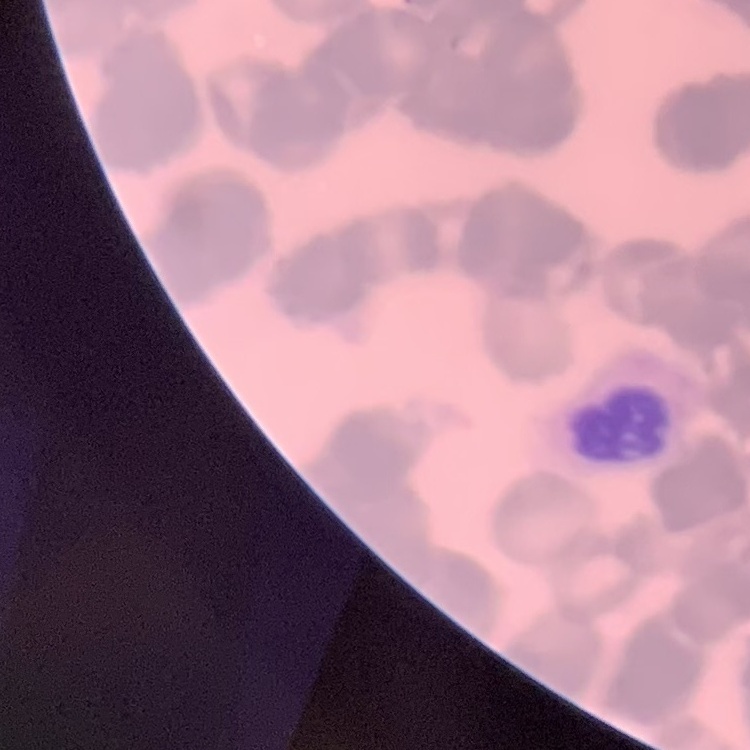
erythrocyte morphology = rouleaux formation
image type = one tile cut from a larger photomicrograph
preparation = thin blood film
stain = Field's or Giemsa